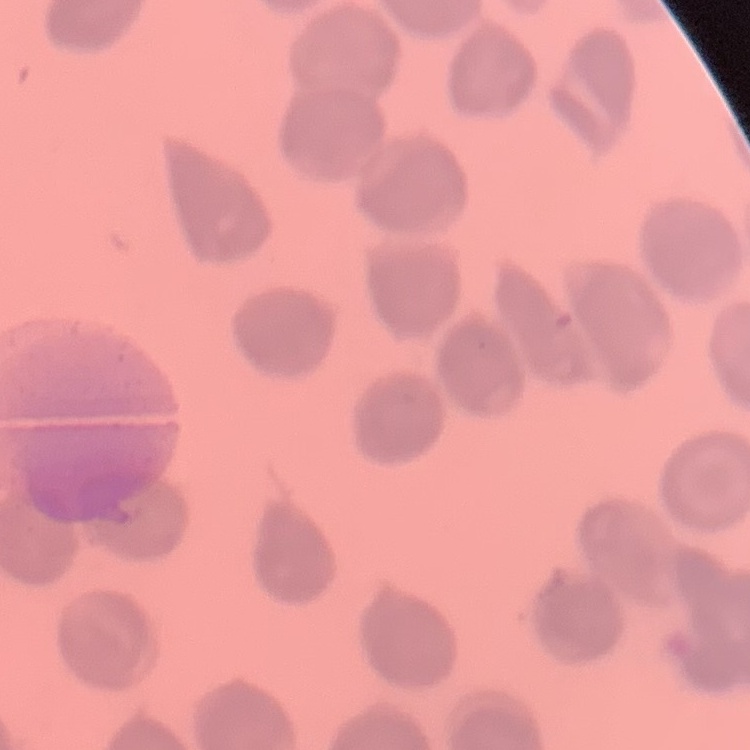 The erythrocytes show no rouleaux formation. Square crop of a larger photomicrograph. Thin peripheral smear. Stained with either Field's or Giemsa.